State which cell type is depicted.
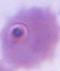
An erythrocyte.

Summary:
  - Magnification: 1000x
  - Modality: photomicrograph